Assess the morphology of the erythrocytes.
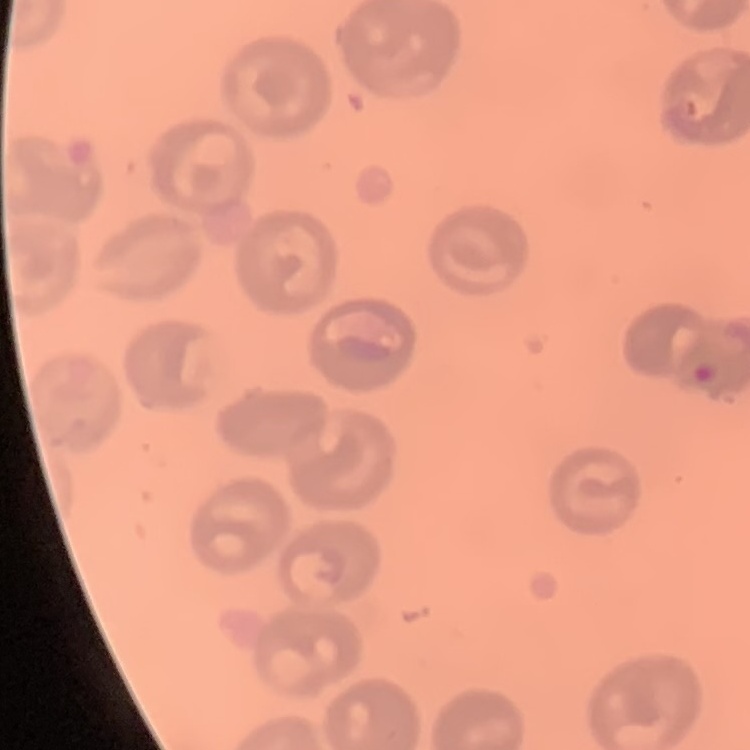
No rouleaux formation.

stain = Field's or Giemsa
image type = one tile cut from a larger photomicrograph
preparation = thin peripheral smear